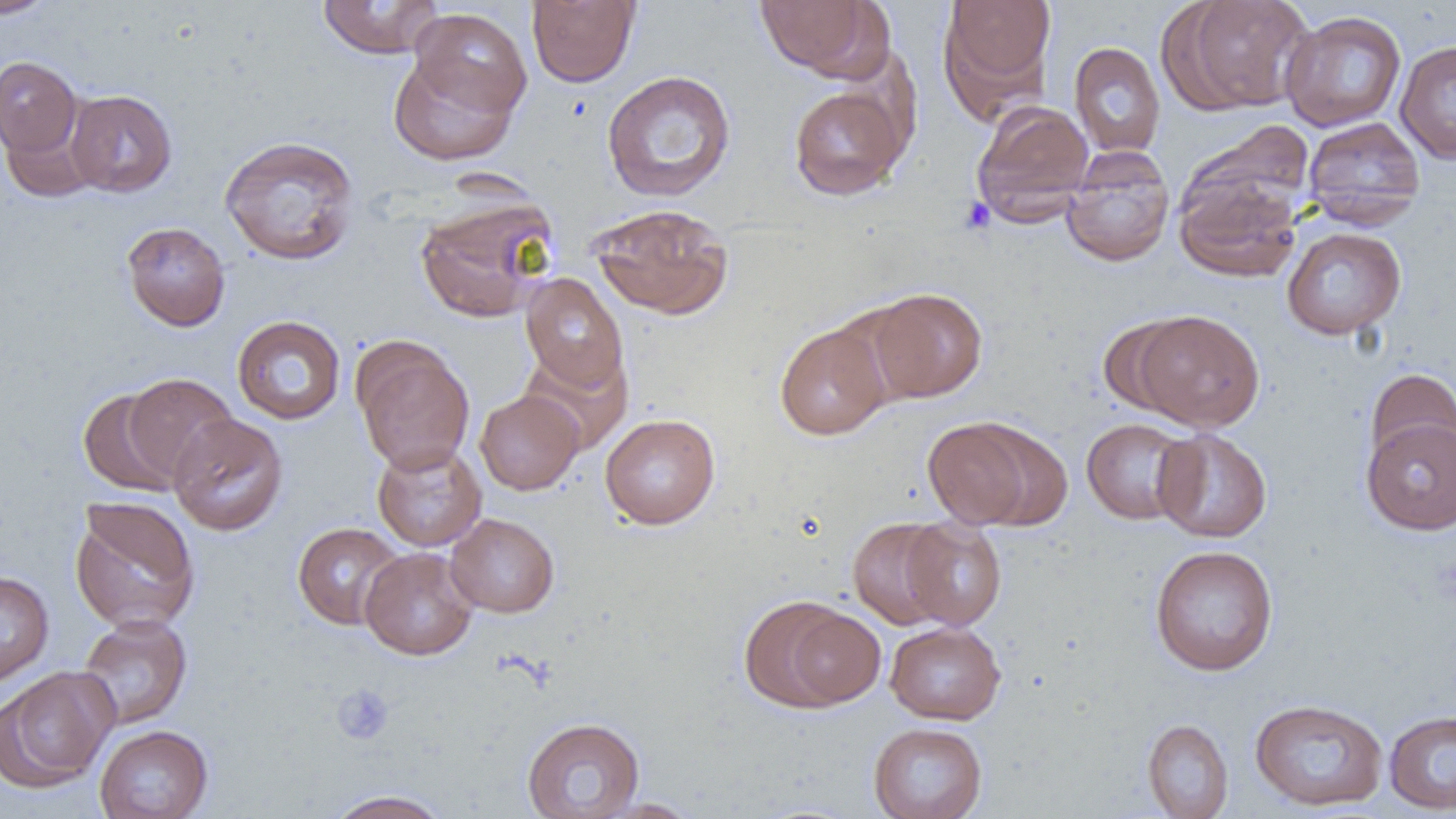

slide-level diagnosis = no evidence of blood parasites
field of view = one of a larger specimen
image size = 1456×819 pixels
uninfected red blood cell locations = approximate bounding boxes as named x1/y1/x2/y2 corners in pixels: (x1=0, y1=0, x2=58, y2=20), (x1=527, y1=0, x2=640, y2=88), (x1=754, y1=0, x2=883, y2=79), (x1=938, y1=0, x2=1057, y2=112), (x1=1170, y1=0, x2=1315, y2=114), (x1=316, y1=1, x2=445, y2=59), (x1=409, y1=7, x2=531, y2=121), (x1=1279, y1=10, x2=1407, y2=132), (x1=1395, y1=39, x2=1456, y2=163), (x1=1069, y1=42, x2=1166, y2=157), (x1=387, y1=49, x2=522, y2=166), (x1=0, y1=56, x2=82, y2=157), (x1=601, y1=69, x2=736, y2=202), (x1=788, y1=83, x2=910, y2=200), (x1=65, y1=89, x2=177, y2=197), (x1=971, y1=100, x2=1095, y2=223), (x1=1302, y1=116, x2=1426, y2=227), (x1=3, y1=120, x2=96, y2=199), (x1=1182, y1=121, x2=1316, y2=227), (x1=219, y1=135, x2=360, y2=266), (x1=1060, y1=148, x2=1174, y2=267), (x1=1173, y1=175, x2=1302, y2=282), (x1=415, y1=195, x2=558, y2=323), (x1=589, y1=204, x2=733, y2=320), (x1=121, y1=221, x2=231, y2=332), (x1=1281, y1=226, x2=1406, y2=340), (x1=520, y1=273, x2=629, y2=392), (x1=865, y1=288, x2=988, y2=402), (x1=1131, y1=309, x2=1266, y2=432), (x1=1096, y1=313, x2=1196, y2=418), (x1=232, y1=315, x2=346, y2=424), (x1=775, y1=321, x2=892, y2=440), (x1=352, y1=338, x2=475, y2=475), (x1=1364, y1=368, x2=1456, y2=471), (x1=121, y1=373, x2=238, y2=485), (x1=77, y1=388, x2=186, y2=496), (x1=474, y1=389, x2=583, y2=495), (x1=167, y1=413, x2=289, y2=536), (x1=599, y1=413, x2=721, y2=529), (x1=923, y1=417, x2=1044, y2=530), (x1=1361, y1=417, x2=1456, y2=536), (x1=1080, y1=418, x2=1197, y2=525), (x1=1152, y1=428, x2=1272, y2=543), (x1=371, y1=441, x2=487, y2=552), (x1=69, y1=496, x2=201, y2=634), (x1=445, y1=513, x2=559, y2=618), (x1=848, y1=517, x2=956, y2=630), (x1=900, y1=518, x2=1007, y2=630), (x1=292, y1=522, x2=406, y2=630), (x1=1149, y1=544, x2=1279, y2=676), (x1=359, y1=547, x2=478, y2=660), (x1=0, y1=571, x2=54, y2=687), (x1=740, y1=594, x2=878, y2=711), (x1=77, y1=614, x2=193, y2=730), (x1=884, y1=621, x2=1006, y2=725), (x1=0, y1=666, x2=119, y2=793), (x1=1249, y1=698, x2=1388, y2=811), (x1=1384, y1=709, x2=1456, y2=814), (x1=521, y1=716, x2=645, y2=818), (x1=1142, y1=718, x2=1234, y2=818), (x1=868, y1=722, x2=988, y2=819), (x1=94, y1=724, x2=213, y2=819), (x1=324, y1=789, x2=453, y2=819), (x1=589, y1=798, x2=703, y2=818)
magnification = 1000x
preparation = thin blood film
platelet locations = approximate bounding boxes as named x1/y1/x2/y2 corners in pixels: (x1=959, y1=196, x2=996, y2=235), (x1=332, y1=683, x2=395, y2=745)
modality = optical microscopy